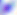

Summary:
  - Identification: Toxoplasma gondii
  - Magnification: 400x
  - Modality: micrograph